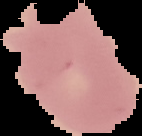

Summary:
  - Image size: 142×136 pixels
  - Preparation: thin blood film
  - Result: negative for malaria parasites
  - Image type: segmented cell region with the area outside set to black